Point out each Plasmodium parasite.
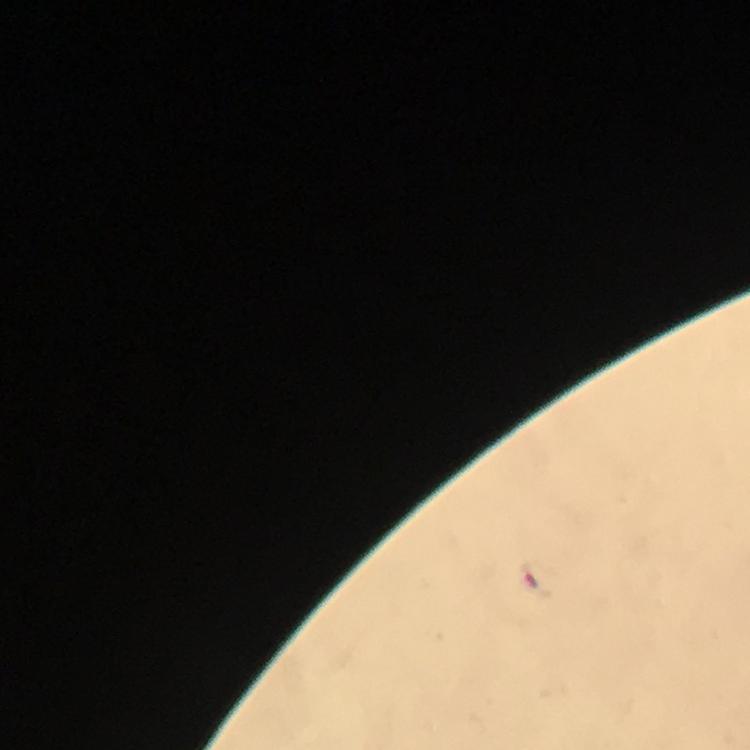

Approximate centers as [x, y] in pixels.
Plasmodium parasites: [537, 579].

100x magnification. Immersion oil was used. Thick blood film. A crop from one field of view. From a malaria diagnostic workup. Smartphone photograph taken through a microscope. Giemsa-stained preparation. Image is 750×750 pixels.